Report the malaria status of this cell.
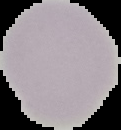

Uninfected.

The area outside the segmented cell region is set to black. Image is 121×130 pixels. From a thin blood film.